State which cell type is depicted.
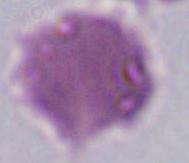
This is an erythrocyte.

Summary:
  - Modality: micrograph
  - Magnification: 1000x